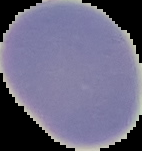
result = no malaria parasites detected
image size = 142×151 pixels
preparation = thin blood smear
image type = cell region segmented out of the field of view; surrounding area masked to black